Assess this cell for malaria.
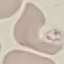
Uninfected.

Summary:
  - Stain: Giemsa
  - Image type: automatically extracted cell patch, resized to 64 × 64 pixels
  - Capture: smartphone through the microscope eyepiece
  - Preparation: thin smear